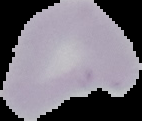
From a thin blood smear. Result: negative for Plasmodium parasites. Cell region segmented out of the field of view; the surrounding area is masked to black. Image is 142×121 pixels.